Name the blood parasite species.
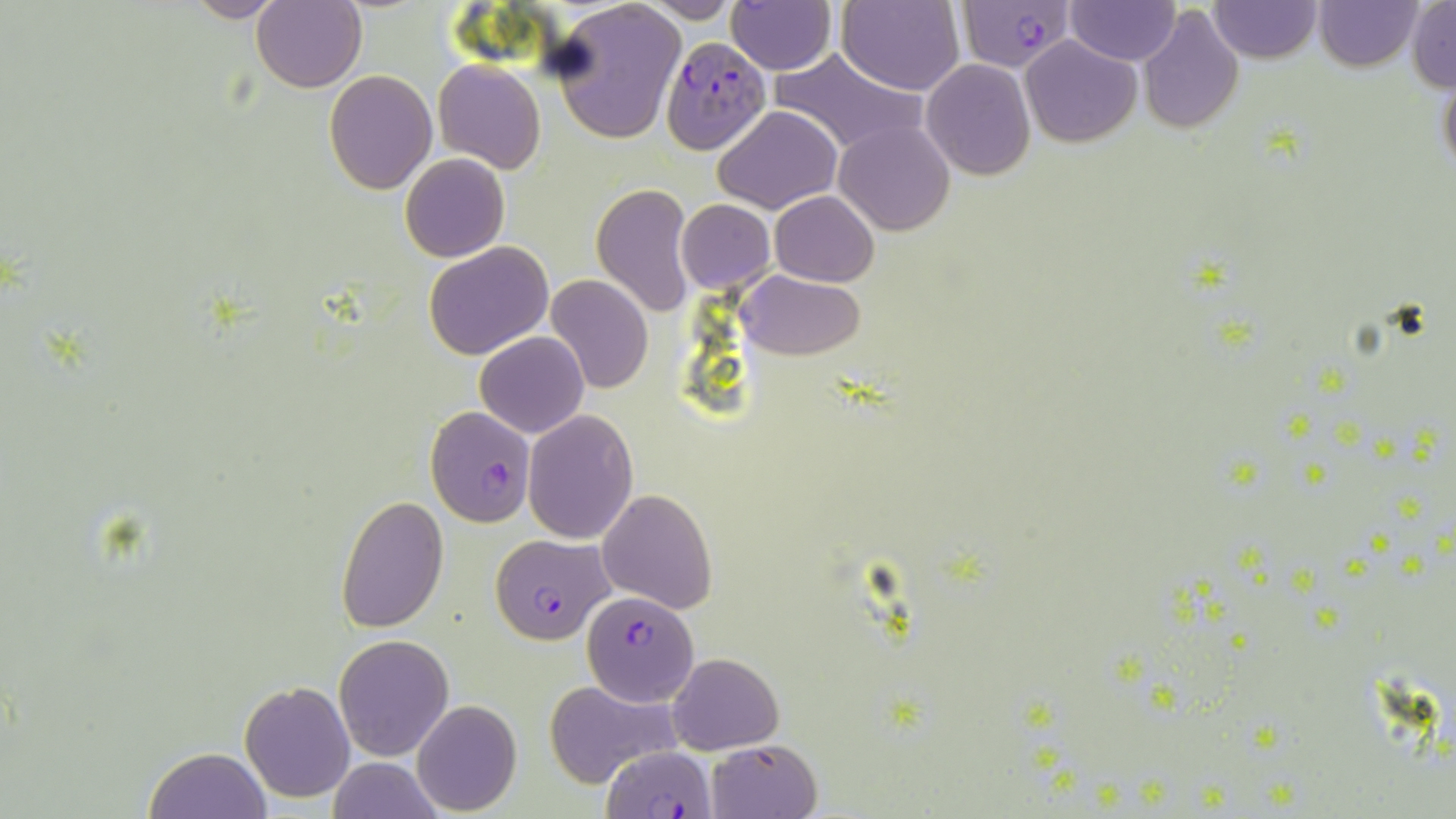

Plasmodium falciparum.

Approximate bounding boxes as (x1, y1, x2, y2) in pixels. Uninfected red blood cell locations: (182, 0, 289, 23), (1315, 0, 1422, 71), (250, 1, 366, 91), (548, 1, 687, 145), (640, 1, 746, 23), (728, 1, 839, 74), (837, 1, 965, 95), (1065, 1, 1180, 66), (1209, 1, 1322, 63), (1408, 2, 1455, 91), (1136, 6, 1245, 134), (1020, 36, 1140, 147), (770, 46, 927, 160), (920, 59, 1037, 182), (433, 60, 546, 173), (1438, 64, 1456, 183), (323, 70, 437, 194), (713, 104, 842, 213), (834, 120, 956, 235), (400, 153, 510, 263), (590, 183, 698, 317), (770, 191, 878, 287), (675, 199, 774, 293), (423, 241, 554, 360), (739, 269, 864, 360), (545, 275, 654, 394), (475, 332, 589, 438), (522, 409, 638, 543), (596, 488, 718, 614), (335, 497, 449, 633), (335, 633, 454, 761), (667, 651, 784, 756), (544, 677, 680, 786), (240, 679, 356, 803), (411, 700, 522, 816), (705, 738, 822, 819), (144, 746, 270, 818), (326, 757, 443, 819). Plasmodium falciparum-infected red blood cell locations: (958, 0, 1075, 72), (660, 36, 769, 155), (425, 407, 537, 527), (490, 533, 615, 645), (583, 590, 698, 707), (600, 743, 720, 819). May-Grünwald-Giemsa stain. One field of a larger specimen. Image is 1456×819 pixels. Thin blood smear. Light microscopy. 1000x magnification.